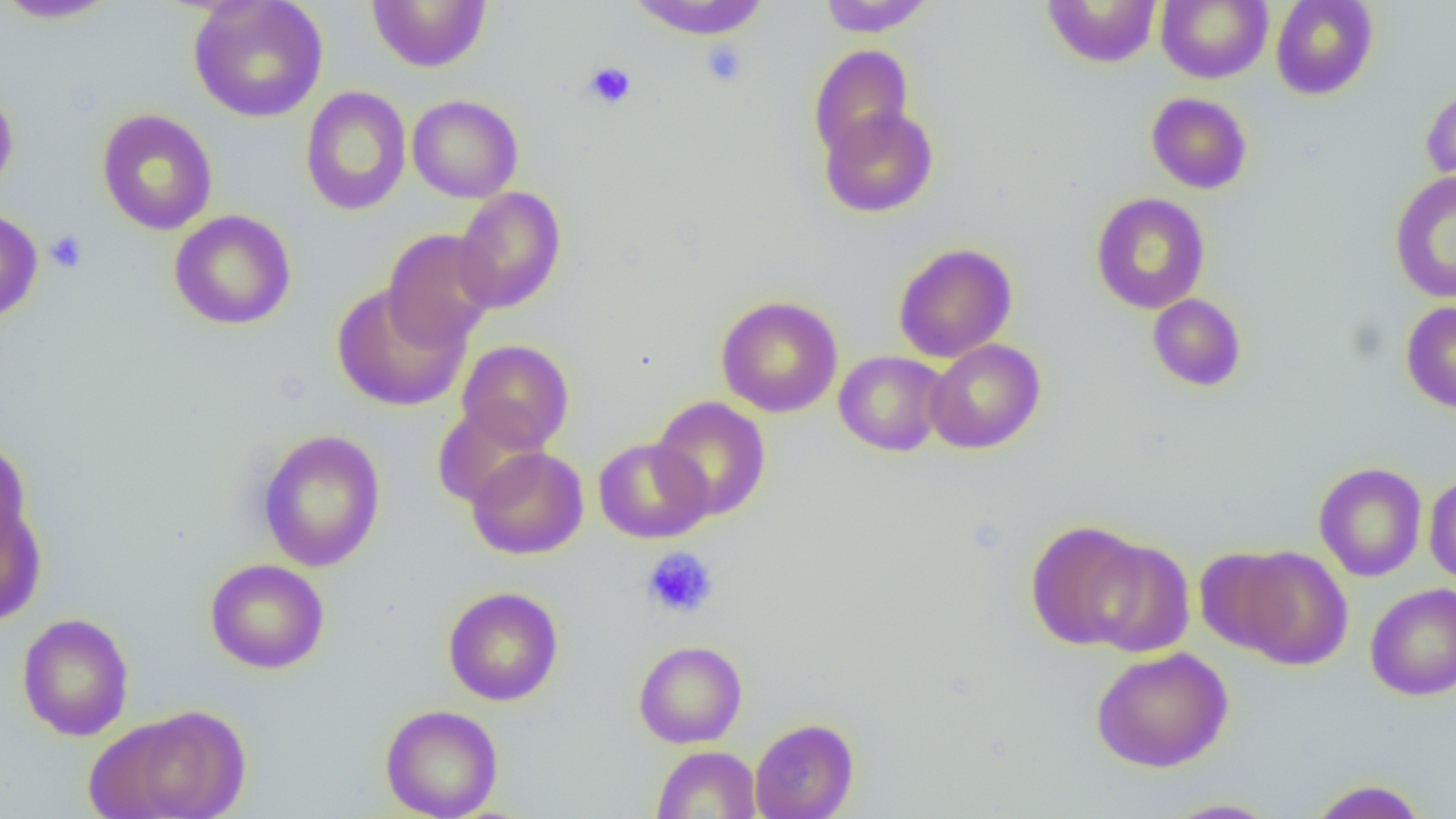
Summary:
  - Coordinate format: approximate bounding boxes as named x1/y1/x2/y2 corners in pixels
  - Uninfected red blood cell locations: (x1=0, y1=0, x2=121, y2=23), (x1=188, y1=0, x2=328, y2=123), (x1=366, y1=0, x2=491, y2=73), (x1=627, y1=0, x2=771, y2=39), (x1=817, y1=0, x2=934, y2=36), (x1=1041, y1=0, x2=1161, y2=68), (x1=1270, y1=0, x2=1378, y2=100), (x1=1157, y1=1, x2=1273, y2=84), (x1=808, y1=44, x2=914, y2=163), (x1=0, y1=84, x2=18, y2=201), (x1=1422, y1=84, x2=1456, y2=194), (x1=300, y1=85, x2=412, y2=216), (x1=1146, y1=92, x2=1253, y2=194), (x1=407, y1=94, x2=524, y2=203), (x1=819, y1=105, x2=939, y2=218), (x1=96, y1=108, x2=218, y2=236), (x1=1389, y1=170, x2=1456, y2=304), (x1=452, y1=186, x2=567, y2=314), (x1=1090, y1=192, x2=1210, y2=314), (x1=0, y1=208, x2=43, y2=325), (x1=169, y1=210, x2=296, y2=330), (x1=383, y1=228, x2=497, y2=350), (x1=893, y1=242, x2=1017, y2=363), (x1=330, y1=283, x2=470, y2=412), (x1=1148, y1=293, x2=1246, y2=392), (x1=716, y1=295, x2=843, y2=418), (x1=1400, y1=300, x2=1456, y2=413), (x1=457, y1=339, x2=575, y2=453), (x1=924, y1=339, x2=1046, y2=454), (x1=833, y1=351, x2=949, y2=457), (x1=650, y1=396, x2=771, y2=521), (x1=432, y1=404, x2=550, y2=510), (x1=258, y1=429, x2=386, y2=572), (x1=593, y1=437, x2=712, y2=543), (x1=1, y1=438, x2=34, y2=566), (x1=466, y1=446, x2=589, y2=560), (x1=1314, y1=462, x2=1427, y2=582), (x1=1424, y1=473, x2=1456, y2=585), (x1=0, y1=498, x2=47, y2=627), (x1=1025, y1=520, x2=1150, y2=651), (x1=1083, y1=538, x2=1196, y2=657), (x1=1225, y1=545, x2=1354, y2=670), (x1=1195, y1=547, x2=1301, y2=660), (x1=205, y1=558, x2=330, y2=674), (x1=1365, y1=583, x2=1456, y2=700), (x1=443, y1=586, x2=563, y2=706), (x1=16, y1=613, x2=134, y2=741), (x1=633, y1=639, x2=747, y2=748), (x1=1090, y1=647, x2=1234, y2=773), (x1=380, y1=704, x2=503, y2=819), (x1=89, y1=705, x2=253, y2=819), (x1=749, y1=718, x2=859, y2=819), (x1=652, y1=745, x2=761, y2=819), (x1=1306, y1=778, x2=1430, y2=818), (x1=1159, y1=798, x2=1282, y2=818)
  - Platelet locations: (x1=701, y1=40, x2=749, y2=87), (x1=584, y1=61, x2=637, y2=109), (x1=45, y1=230, x2=88, y2=274), (x1=642, y1=547, x2=719, y2=619)
  - Slide-level diagnosis: negative for blood parasites
  - Field of view: one of a larger specimen
  - Magnification: 1000x
  - Image size: 1456×819 pixels
  - Preparation: thin blood film
  - Modality: optical microscopy